Classify this cell by malaria status.
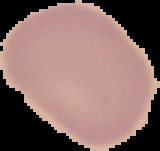
Uninfected.

image type = segmented cell region with the area outside set to black
image size = 160×151 pixels
preparation = thin blood smear